Assess this cell for malaria.
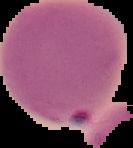
Parasitized.

image type = segmented cell region on a black background
preparation = thin blood smear
image size = 133×148 pixels